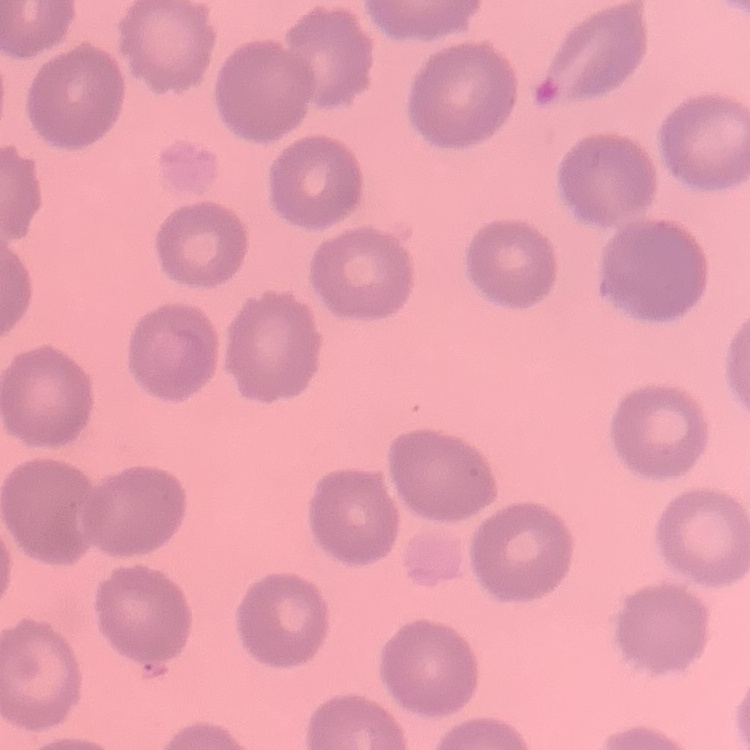

{
  "red_blood_cell_morphology": "no rouleaux formation",
  "stain": "Field's or Giemsa",
  "image_type": "one tile cut from a larger photomicrograph",
  "preparation": "thin blood smear"
}